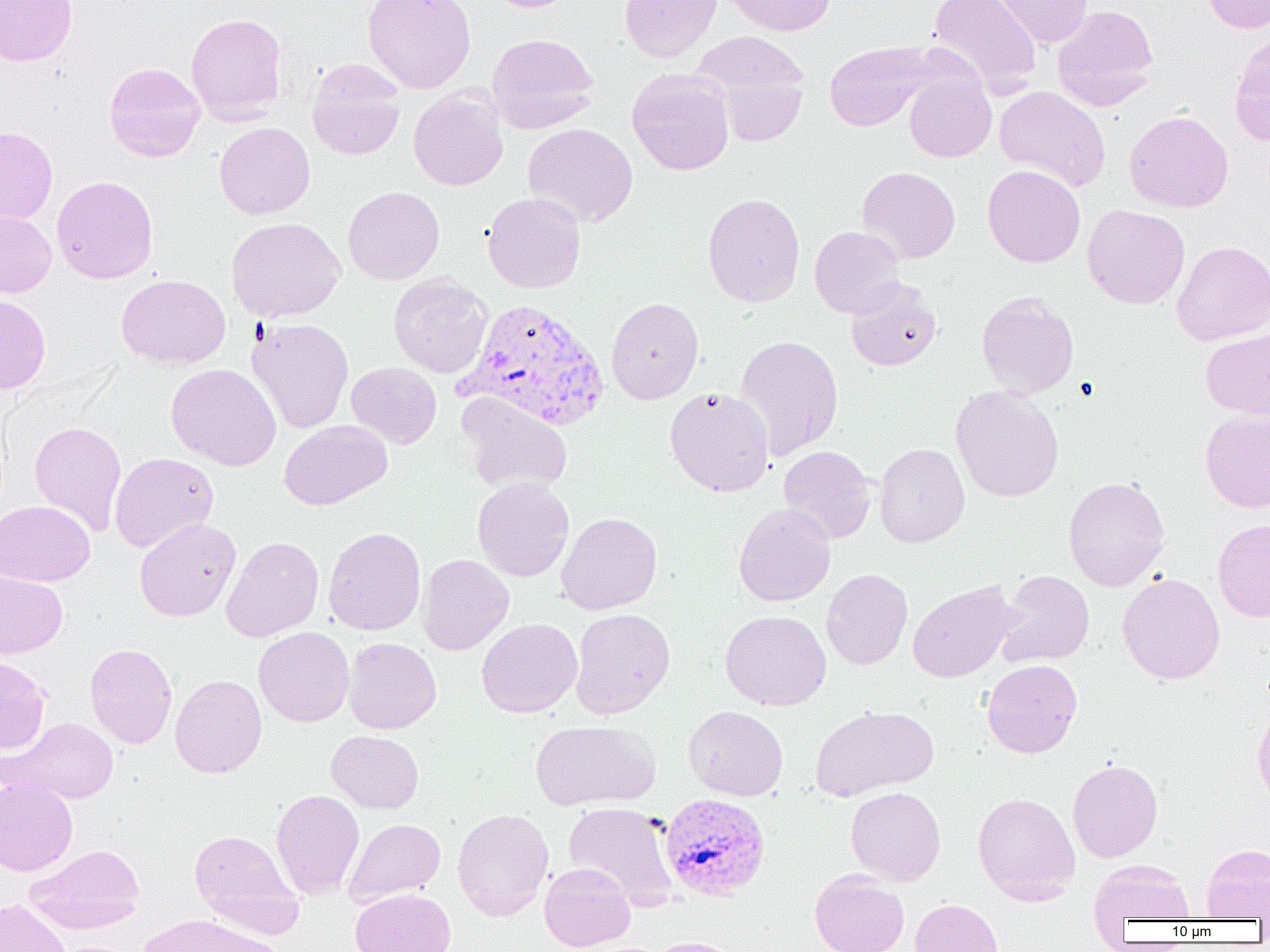
Approximate bounding boxes as named x1/y1/x2/y2 corners in pixels. Plasmodium vivax-infected red blood cell locations: (x1=458, y1=298, x2=610, y2=431), (x1=661, y1=794, x2=771, y2=900). Uninfected red blood cell locations: (x1=0, y1=0, x2=78, y2=66), (x1=363, y1=0, x2=476, y2=94), (x1=481, y1=0, x2=581, y2=13), (x1=620, y1=0, x2=722, y2=63), (x1=723, y1=0, x2=837, y2=36), (x1=928, y1=0, x2=1042, y2=97), (x1=990, y1=0, x2=1093, y2=48), (x1=1200, y1=0, x2=1270, y2=34), (x1=1052, y1=5, x2=1158, y2=111), (x1=185, y1=13, x2=287, y2=124), (x1=692, y1=31, x2=811, y2=136), (x1=486, y1=33, x2=600, y2=134), (x1=1229, y1=33, x2=1270, y2=146), (x1=824, y1=41, x2=935, y2=132), (x1=307, y1=59, x2=406, y2=160), (x1=104, y1=62, x2=205, y2=162), (x1=627, y1=68, x2=734, y2=176), (x1=904, y1=72, x2=996, y2=163), (x1=995, y1=86, x2=1111, y2=192), (x1=408, y1=87, x2=508, y2=190), (x1=1124, y1=110, x2=1234, y2=213), (x1=215, y1=122, x2=315, y2=219), (x1=523, y1=123, x2=638, y2=228), (x1=0, y1=126, x2=58, y2=224), (x1=982, y1=165, x2=1085, y2=267), (x1=857, y1=166, x2=960, y2=264), (x1=51, y1=175, x2=158, y2=284), (x1=343, y1=186, x2=445, y2=285), (x1=482, y1=192, x2=586, y2=293), (x1=703, y1=192, x2=805, y2=308), (x1=1082, y1=204, x2=1190, y2=309), (x1=0, y1=208, x2=57, y2=298), (x1=226, y1=218, x2=345, y2=322), (x1=809, y1=226, x2=906, y2=318), (x1=1171, y1=240, x2=1270, y2=345), (x1=388, y1=273, x2=493, y2=378), (x1=116, y1=275, x2=230, y2=369), (x1=845, y1=278, x2=942, y2=372), (x1=976, y1=291, x2=1079, y2=399), (x1=0, y1=295, x2=51, y2=394), (x1=606, y1=297, x2=704, y2=404), (x1=246, y1=317, x2=354, y2=434), (x1=1201, y1=328, x2=1270, y2=418), (x1=734, y1=334, x2=844, y2=460), (x1=346, y1=362, x2=442, y2=449), (x1=166, y1=363, x2=281, y2=470), (x1=951, y1=385, x2=1064, y2=503), (x1=665, y1=386, x2=775, y2=497), (x1=458, y1=394, x2=572, y2=495), (x1=1200, y1=411, x2=1270, y2=513), (x1=279, y1=420, x2=392, y2=510), (x1=29, y1=421, x2=127, y2=536), (x1=874, y1=443, x2=970, y2=548), (x1=778, y1=445, x2=876, y2=543), (x1=110, y1=452, x2=219, y2=552), (x1=1063, y1=476, x2=1170, y2=591), (x1=472, y1=477, x2=574, y2=582), (x1=0, y1=501, x2=95, y2=586), (x1=734, y1=503, x2=835, y2=607), (x1=556, y1=512, x2=663, y2=615), (x1=135, y1=518, x2=240, y2=621), (x1=1213, y1=519, x2=1270, y2=622), (x1=324, y1=526, x2=426, y2=635), (x1=220, y1=535, x2=324, y2=642), (x1=416, y1=554, x2=514, y2=655), (x1=0, y1=569, x2=67, y2=659), (x1=822, y1=569, x2=913, y2=670), (x1=995, y1=570, x2=1095, y2=668), (x1=1117, y1=573, x2=1225, y2=684), (x1=908, y1=581, x2=1019, y2=682), (x1=569, y1=608, x2=675, y2=719), (x1=720, y1=610, x2=831, y2=710), (x1=476, y1=618, x2=582, y2=718), (x1=254, y1=626, x2=354, y2=727), (x1=344, y1=637, x2=441, y2=734), (x1=85, y1=643, x2=178, y2=748), (x1=0, y1=656, x2=51, y2=753), (x1=981, y1=659, x2=1082, y2=758), (x1=170, y1=674, x2=267, y2=778), (x1=1252, y1=704, x2=1270, y2=808), (x1=683, y1=705, x2=788, y2=801), (x1=810, y1=705, x2=939, y2=801), (x1=9, y1=717, x2=119, y2=803), (x1=530, y1=720, x2=660, y2=811), (x1=327, y1=730, x2=424, y2=813), (x1=1067, y1=759, x2=1163, y2=862), (x1=0, y1=777, x2=78, y2=875), (x1=845, y1=786, x2=946, y2=886), (x1=271, y1=788, x2=365, y2=900), (x1=973, y1=792, x2=1080, y2=904), (x1=563, y1=802, x2=678, y2=906), (x1=452, y1=808, x2=553, y2=921), (x1=344, y1=818, x2=445, y2=906), (x1=189, y1=830, x2=304, y2=936), (x1=26, y1=843, x2=145, y2=933), (x1=1201, y1=843, x2=1270, y2=920), (x1=1089, y1=859, x2=1194, y2=926), (x1=539, y1=863, x2=635, y2=951), (x1=810, y1=870, x2=909, y2=952), (x1=350, y1=888, x2=456, y2=952), (x1=910, y1=898, x2=1003, y2=952), (x1=0, y1=899, x2=72, y2=952), (x1=138, y1=915, x2=282, y2=952), (x1=645, y1=936, x2=743, y2=952). Slide-level diagnosis: Plasmodium vivax. 1000x magnification. One field of a larger specimen. Image is 1270×952 pixels. Optical microscopy. Thin blood film.